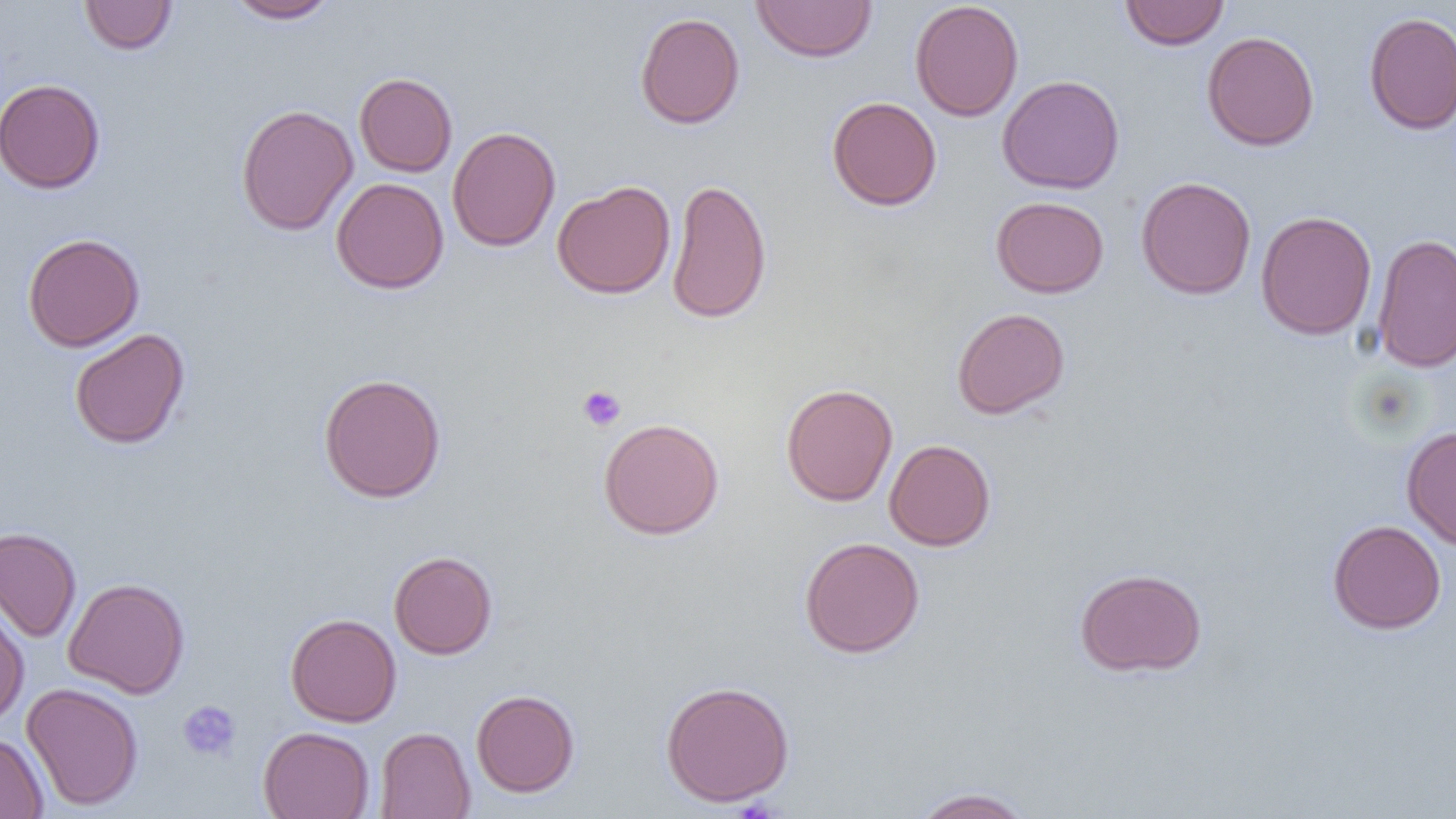

Summary:
  - Coordinate format: approximate bounding boxes as named x1/y1/x2/y2 corners in pixels
  - Uninfected red blood cell locations: (x1=79, y1=0, x2=177, y2=55), (x1=225, y1=0, x2=338, y2=23), (x1=1120, y1=0, x2=1230, y2=50), (x1=751, y1=1, x2=878, y2=63), (x1=910, y1=1, x2=1024, y2=122), (x1=635, y1=11, x2=745, y2=129), (x1=1364, y1=12, x2=1456, y2=135), (x1=1202, y1=30, x2=1319, y2=151), (x1=354, y1=72, x2=457, y2=177), (x1=997, y1=75, x2=1125, y2=194), (x1=1, y1=78, x2=106, y2=194), (x1=827, y1=96, x2=942, y2=210), (x1=235, y1=104, x2=358, y2=236), (x1=447, y1=126, x2=561, y2=252), (x1=1135, y1=176, x2=1256, y2=300), (x1=331, y1=177, x2=449, y2=294), (x1=667, y1=177, x2=772, y2=324), (x1=551, y1=180, x2=676, y2=299), (x1=991, y1=196, x2=1109, y2=297), (x1=1255, y1=210, x2=1377, y2=340), (x1=22, y1=233, x2=144, y2=352), (x1=1371, y1=233, x2=1456, y2=374), (x1=952, y1=307, x2=1070, y2=419), (x1=69, y1=328, x2=190, y2=449), (x1=318, y1=372, x2=447, y2=503), (x1=781, y1=383, x2=898, y2=507), (x1=598, y1=417, x2=725, y2=540), (x1=1401, y1=426, x2=1456, y2=550), (x1=884, y1=439, x2=996, y2=551), (x1=1327, y1=519, x2=1446, y2=634), (x1=0, y1=527, x2=82, y2=642), (x1=799, y1=536, x2=925, y2=658), (x1=388, y1=550, x2=498, y2=659), (x1=1075, y1=567, x2=1207, y2=677), (x1=63, y1=577, x2=190, y2=698), (x1=0, y1=601, x2=29, y2=727), (x1=285, y1=612, x2=402, y2=727), (x1=659, y1=680, x2=795, y2=807), (x1=22, y1=682, x2=144, y2=811), (x1=471, y1=689, x2=580, y2=797), (x1=258, y1=726, x2=375, y2=819), (x1=375, y1=727, x2=475, y2=819), (x1=0, y1=732, x2=48, y2=819), (x1=910, y1=787, x2=1036, y2=818)
  - Platelet locations: (x1=578, y1=385, x2=626, y2=432), (x1=177, y1=700, x2=241, y2=761)
  - Slide-level diagnosis: negative for blood parasites
  - Magnification: 1000x
  - Image size: 1456×819 pixels
  - Modality: optical microscopy
  - Preparation: thin blood smear
  - Field of view: single